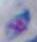 1000x magnification. Toxoplasma gondii is shown. Micrograph.